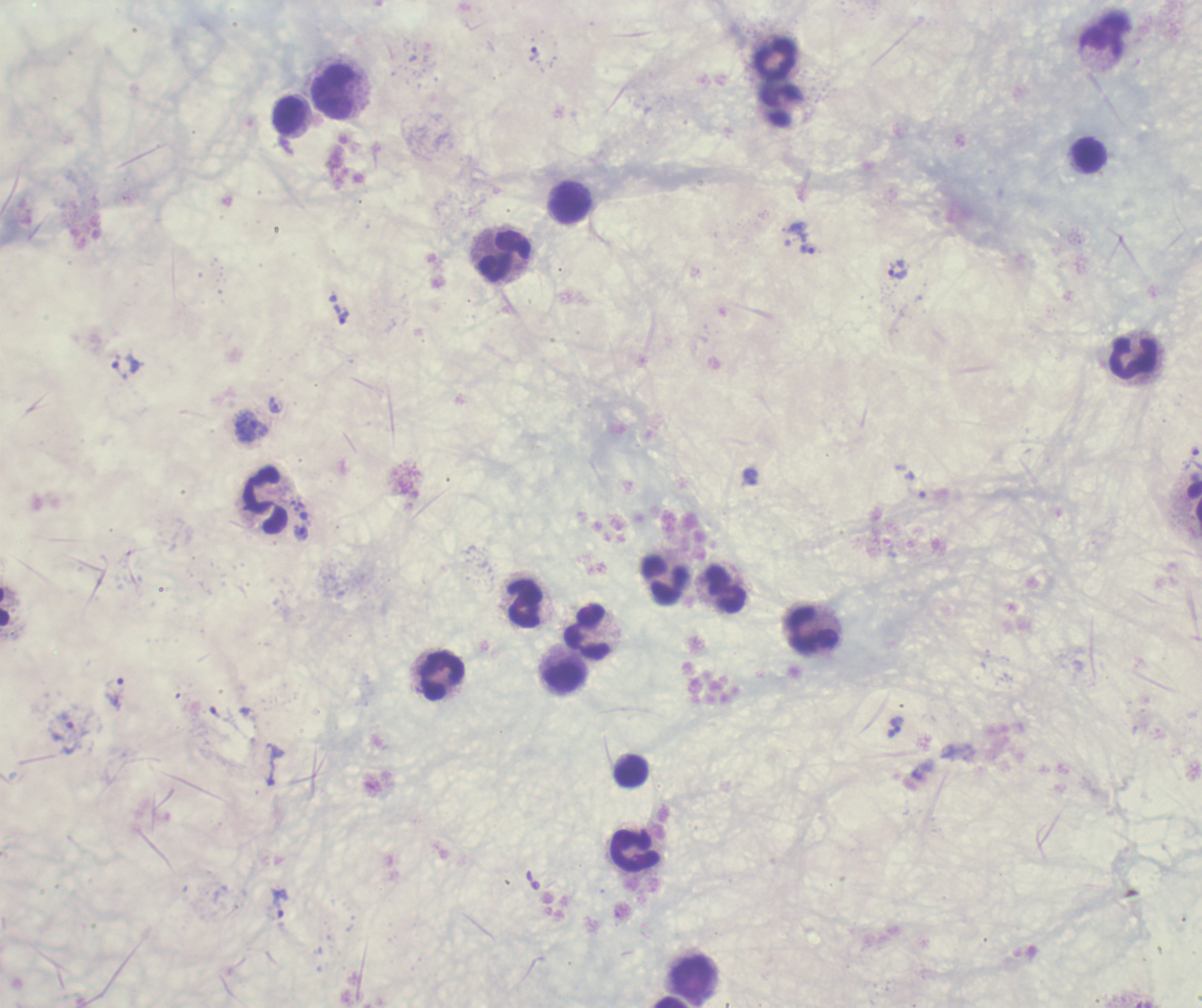

Approximate centers as {x, y} in pixels. Leukocyte locations: {775, 58}, {333, 91}, {781, 104}, {289, 116}, {1089, 155}, {571, 203}, {504, 255}, {1133, 358}, {266, 501}, {666, 580}, {725, 590}, {525, 604}, {815, 629}, {587, 633}, {565, 674}, {442, 676}, {631, 771}, {635, 850}, {693, 977}. Trophozoite locations: {533, 54}, {808, 249}, {899, 269}, {341, 314}, {125, 366}, {276, 406}, {302, 534}, {114, 692}, {894, 727}, {70, 738}, {275, 765}, {280, 903}. Romanowsky-stained preparation. Background quality: poor. Previously used in an actual diagnosis. Coloration quality: bad. Image is 1202×1008 pixels. Single field of view. Result: Plasmodium parasites detected. Thick blood smear. Captured at 100x magnification.